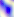

Captured at 400x magnification. Micrograph. Toxoplasma gondii is shown.